Assess this cell for malaria.
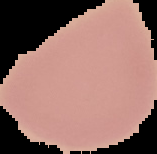

It is uninfected.

The area outside the segmented cell region is set to black. Image is 157×154 pixels. From a thin blood film.